Give the position of every leukocyte visible.
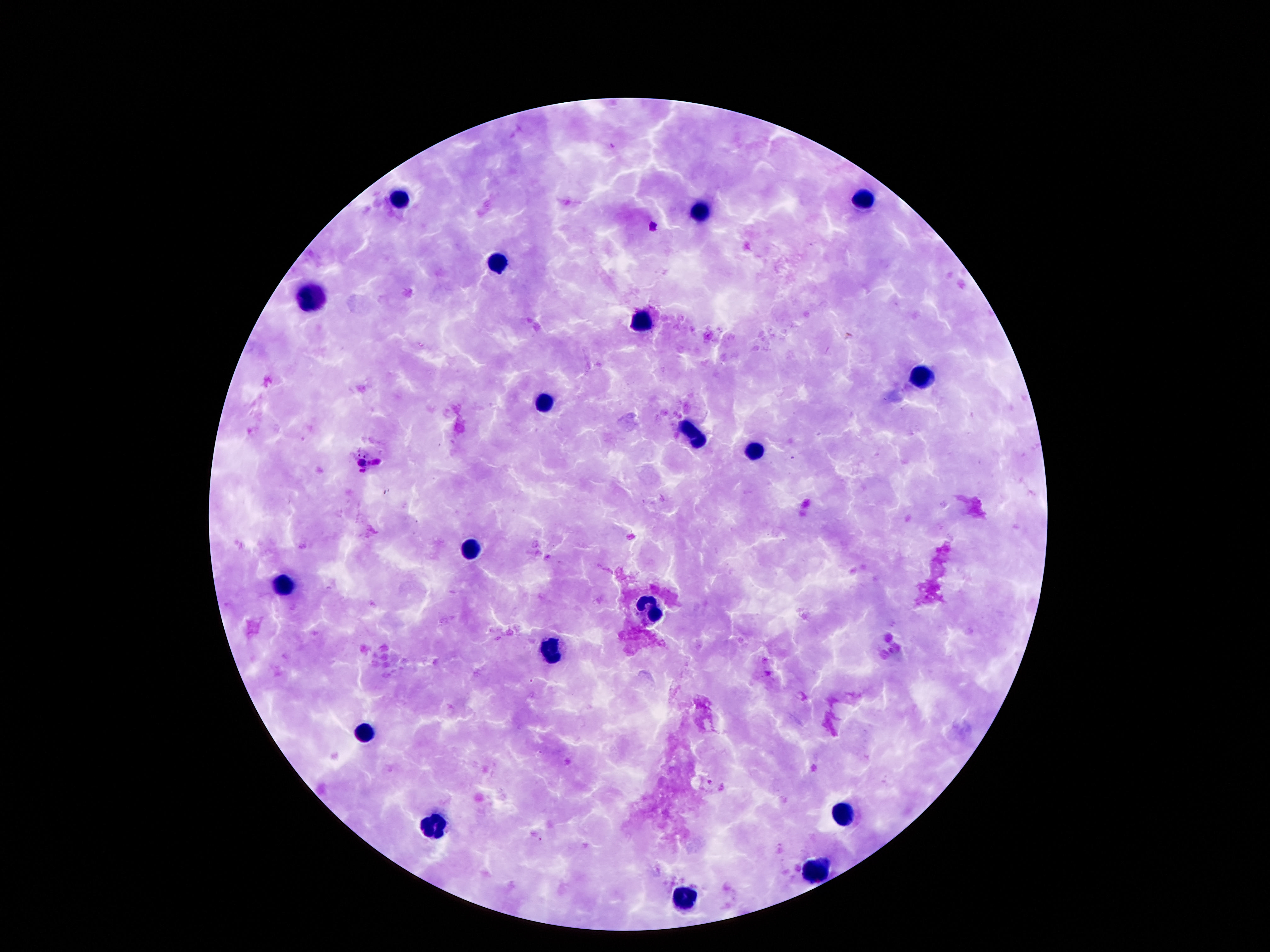
Approximate centers as [x, y] in pixels.
Leukocytes: [399, 201], [862, 201], [700, 212], [494, 264], [313, 297], [639, 320], [920, 380], [543, 404], [690, 436], [756, 451], [471, 550], [283, 586], [649, 609], [547, 651], [363, 732], [840, 815], [430, 826], [817, 870], [682, 900].

magnification = 100x
image size = 1270×952 pixels
capture = smartphone camera through the microscope eyepiece
field of view = single
stain = Giemsa
preparation = thick peripheral-blood smear
patient malaria status = negative